Point out every malaria parasite and every leukocyte.
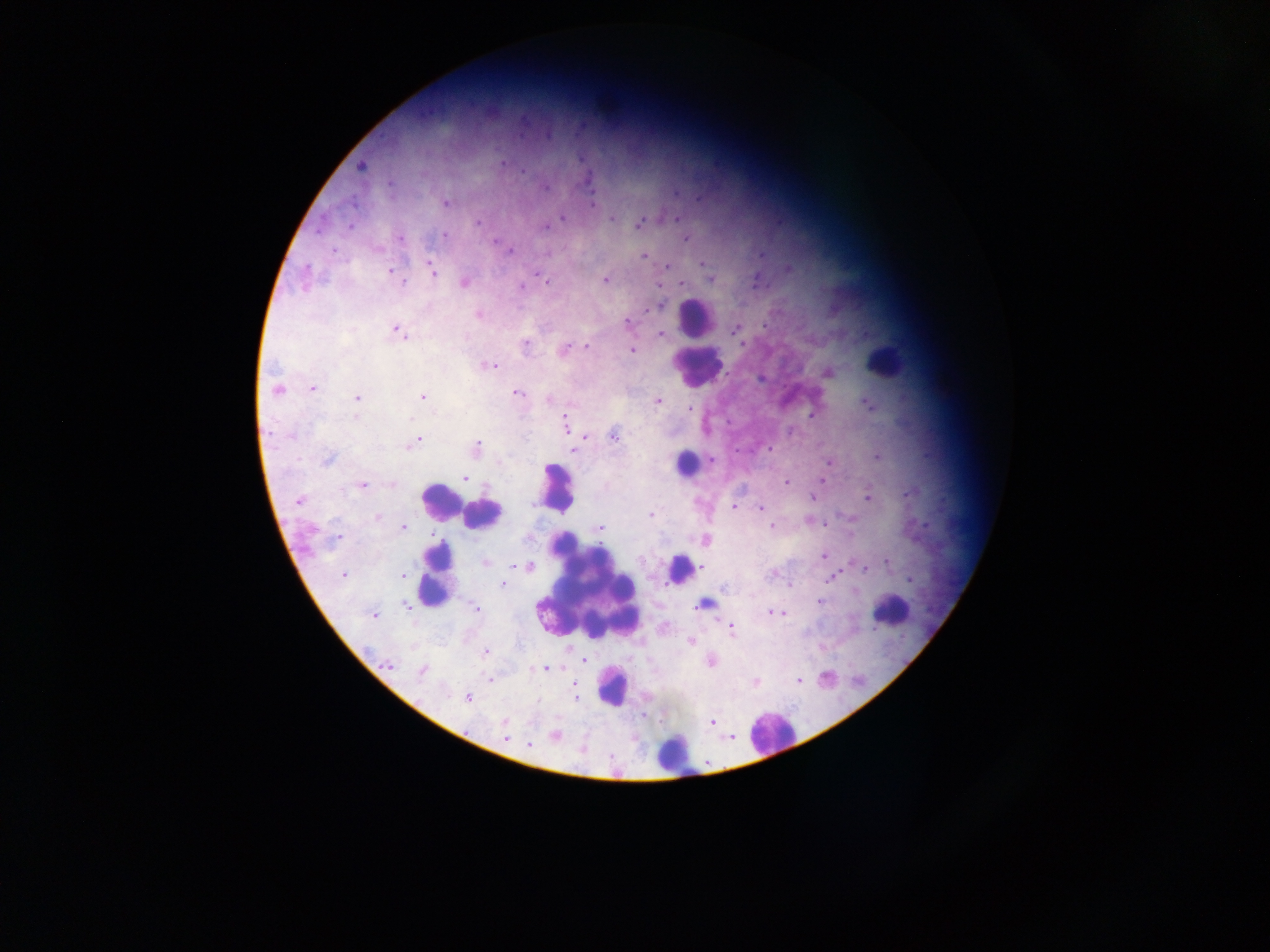
Approximate centers as {x, y} in pixels.
Malaria parasites: {361, 165}, {677, 193}, {697, 198}, {446, 202}, {592, 203}, {562, 217}, {612, 218}, {678, 218}, {640, 222}, {349, 226}, {544, 226}, {444, 235}, {685, 237}, {399, 238}, {334, 251}, {645, 255}, {760, 256}, {701, 264}, {667, 265}, {788, 269}, {431, 270}, {392, 272}, {536, 272}, {397, 276}, {304, 278}, {605, 279}, {711, 280}, {464, 282}, {682, 282}, {520, 287}, {478, 314}, {627, 323}, {736, 329}, {397, 330}, {660, 333}, {741, 344}, {524, 345}, {586, 346}, {564, 349}, {631, 350}, {488, 366}, {827, 373}, {313, 388}, {277, 389}, {517, 392}, {357, 397}, {423, 397}, {549, 399}, {656, 399}, {869, 406}, {687, 408}, {813, 414}, {566, 425}, {584, 435}, {614, 436}, {417, 440}, {476, 448}, {768, 448}, {573, 449}, {876, 456}, {328, 460}, {711, 460}, {828, 462}, {465, 478}, {821, 479}, {786, 482}, {361, 485}, {910, 492}, {814, 497}, {868, 497}, {299, 501}, {733, 507}, {759, 509}, {650, 514}, {377, 517}, {403, 526}, {773, 527}, {600, 528}, {338, 537}, {704, 540}, {822, 557}, {887, 561}, {486, 562}, {527, 566}, {702, 567}, {863, 568}, {772, 574}, {344, 575}, {831, 578}, {909, 580}, {503, 583}, {790, 583}, {854, 590}, {820, 601}, {405, 604}, {703, 604}, {476, 608}, {770, 612}, {783, 613}, {374, 614}, {730, 625}, {692, 641}, {485, 652}, {584, 659}, {710, 661}, {387, 666}, {546, 668}, {422, 670}, {489, 679}, {799, 679}, {755, 683}, {576, 688}, {467, 697}, {576, 698}, {711, 723}, {504, 725}, {556, 735}, {729, 737}, {507, 739}, {529, 745}.
Leukocytes: {693, 318}, {883, 361}, {696, 367}, {684, 463}, {556, 487}, {440, 502}, {483, 515}, {678, 569}, {435, 574}, {588, 588}, {890, 610}, {611, 688}, {769, 734}, {675, 753}.

Summary:
  - Preparation: thick blood smear
  - Image size: 1270×952 pixels
  - Capture: mobile-phone photograph through a microscope
  - Field of view: single
  - Country: Ghana